Assess the morphology of the red blood cells.
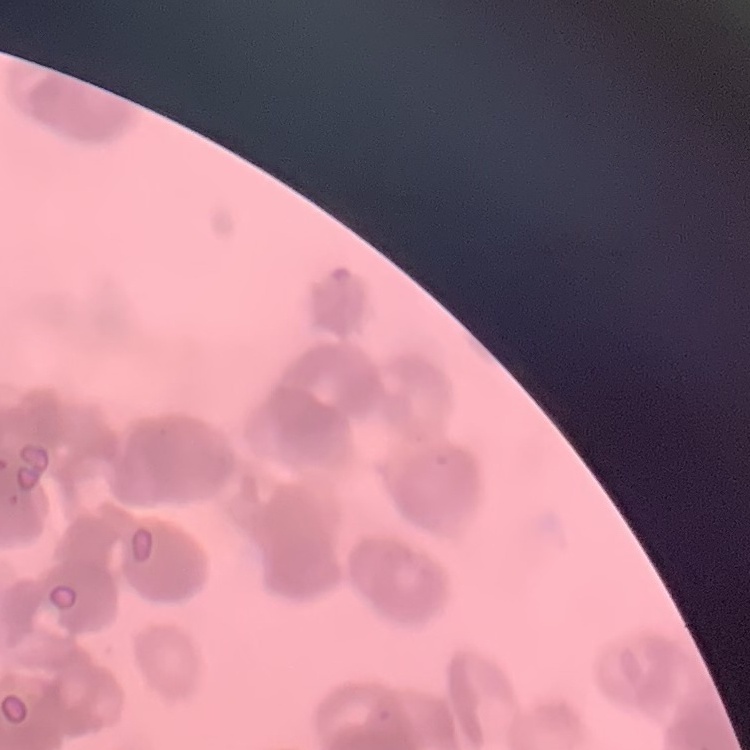
They show rouleaux formation.

image type = one tile cut from a larger photomicrograph
preparation = thin blood smear
stain = Field's or Giemsa